Name the blood parasite species.
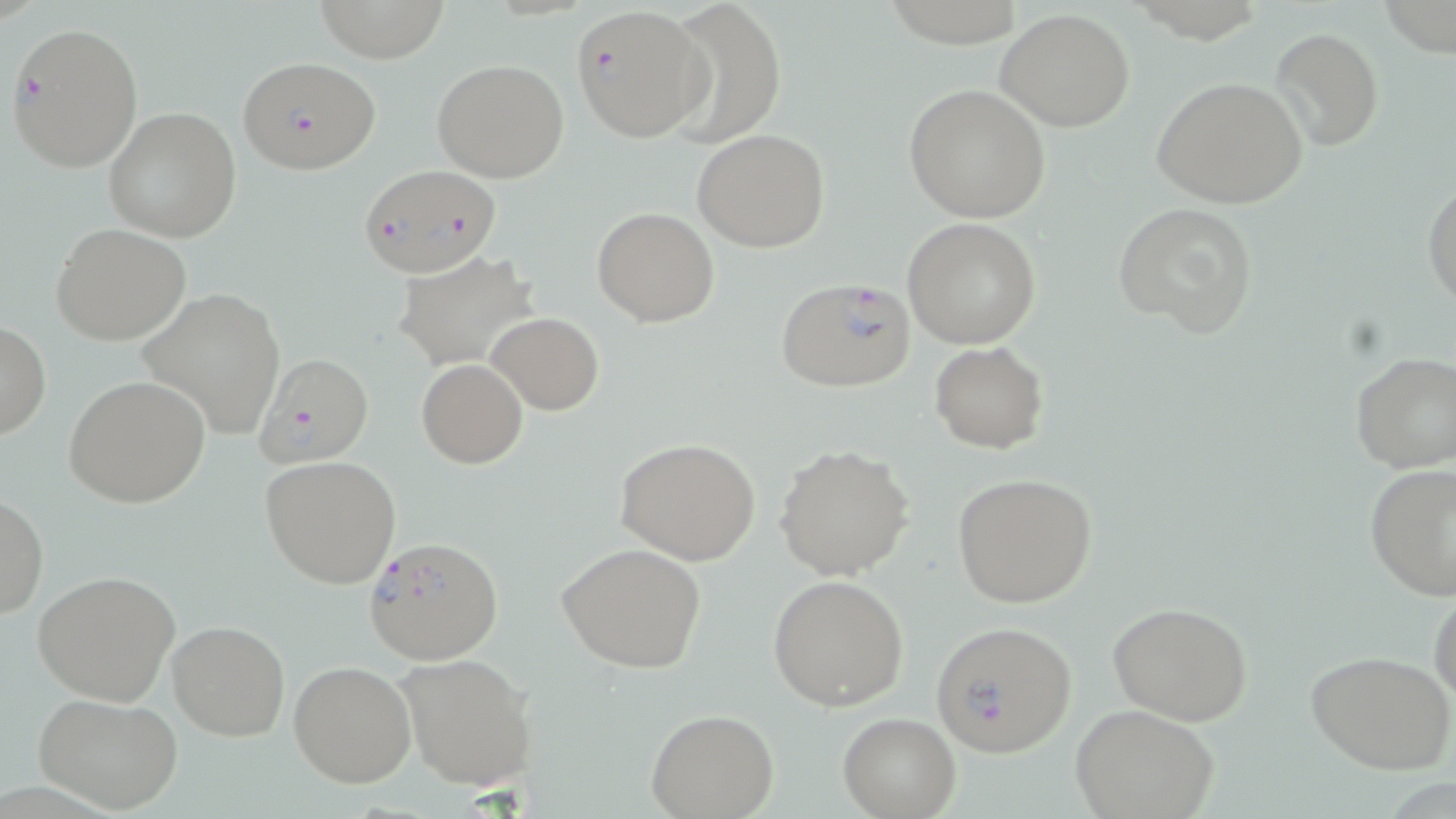
Plasmodium falciparum.

Approximate bounding boxes as [x1, y1, x2, y2] in pixels. Plasmodium falciparum-infected red blood cell locations: [570, 5, 709, 143], [6, 19, 144, 173], [237, 56, 382, 174], [357, 164, 504, 279], [774, 276, 917, 393], [255, 353, 376, 470], [363, 536, 503, 664], [931, 620, 1077, 757]. Uninfected red blood cell locations: [313, 0, 448, 58], [660, 0, 788, 145], [1382, 0, 1456, 56], [996, 8, 1135, 131], [1268, 27, 1382, 152], [431, 59, 570, 184], [1152, 76, 1308, 211], [902, 83, 1051, 225], [103, 107, 242, 243], [692, 127, 829, 251], [1423, 180, 1456, 309], [1113, 200, 1260, 339], [592, 207, 720, 327], [903, 218, 1041, 349], [51, 223, 192, 347], [395, 252, 540, 369], [138, 288, 287, 441], [485, 312, 605, 415], [0, 321, 50, 440], [929, 341, 1049, 453], [1349, 351, 1456, 473], [416, 359, 529, 469], [63, 374, 210, 509], [613, 437, 762, 566], [773, 444, 915, 581], [260, 455, 402, 589], [1364, 463, 1456, 599], [951, 472, 1098, 609], [1, 494, 49, 621], [556, 542, 707, 674], [33, 568, 181, 707], [767, 575, 909, 711], [1430, 580, 1456, 709], [1107, 602, 1253, 725], [168, 619, 290, 739], [1306, 649, 1456, 775], [394, 651, 536, 791], [289, 661, 417, 787], [32, 691, 185, 816], [1072, 706, 1219, 819], [647, 709, 778, 817], [837, 713, 961, 818]. Optical microscopy. Image is 1456×819 pixels. One field of a larger specimen. Thin blood smear. May-Grünwald-Giemsa stain. Captured at 1000x magnification.